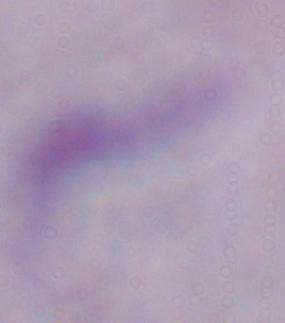
modality = photomicrograph
identification = trypanosome
magnification = 1000x